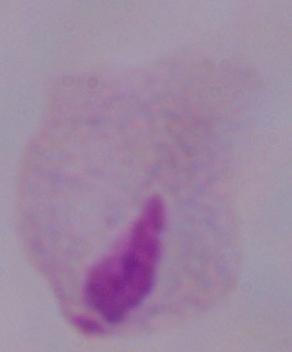
1000x magnification. Photomicrograph. A trichomonad is seen.